Give the extent of all Plasmodium falciparum-infected red blood cells.
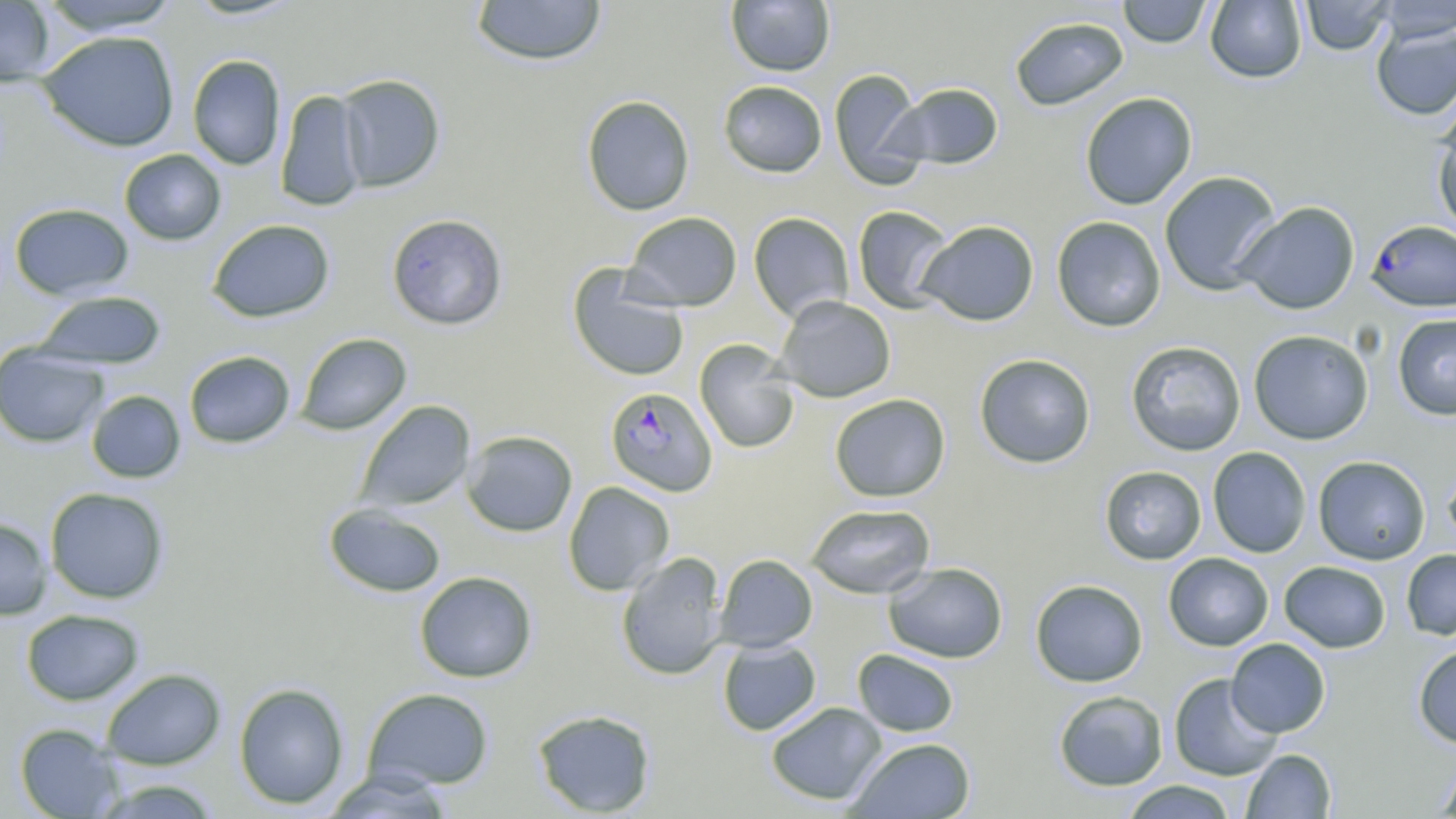

Approximate bounding boxes as (x1, y1, x2, y2) in pixels.
Plasmodium falciparum-infected red blood cells: (1365, 219, 1456, 312), (605, 387, 717, 497).

Uninfected red blood cell locations: (469, 0, 607, 67), (725, 0, 836, 76), (1118, 0, 1212, 48), (1205, 0, 1307, 83), (1299, 0, 1395, 56), (1375, 0, 1456, 42), (0, 1, 56, 86), (37, 1, 182, 35), (1009, 16, 1129, 112), (1371, 23, 1456, 120), (38, 30, 180, 152), (187, 54, 286, 170), (830, 69, 928, 186), (335, 74, 445, 192), (718, 80, 827, 177), (885, 82, 1004, 171), (275, 90, 367, 211), (1079, 92, 1198, 210), (581, 94, 696, 215), (1432, 112, 1456, 235), (119, 149, 227, 246), (1159, 171, 1282, 295), (1234, 201, 1360, 314), (9, 202, 135, 300), (852, 205, 956, 314), (623, 212, 742, 311), (748, 212, 855, 323), (386, 213, 508, 330), (1051, 216, 1167, 332), (207, 219, 335, 323), (916, 220, 1039, 326), (568, 265, 690, 382), (34, 290, 166, 370), (774, 295, 896, 402), (1392, 313, 1456, 420), (1248, 329, 1374, 445), (295, 332, 411, 435), (694, 339, 800, 454), (1126, 340, 1246, 456), (0, 344, 108, 448), (184, 350, 295, 448), (974, 353, 1096, 469), (86, 390, 186, 483), (829, 394, 951, 502), (355, 400, 475, 512), (462, 430, 577, 537), (1207, 446, 1312, 557), (1313, 455, 1431, 565), (1443, 461, 1456, 554), (1099, 465, 1206, 565), (563, 481, 675, 596), (45, 487, 169, 604), (324, 503, 447, 598), (806, 503, 936, 599), (0, 518, 52, 619), (1401, 549, 1456, 640), (615, 551, 728, 681), (1163, 553, 1273, 651), (714, 554, 818, 652), (1279, 560, 1391, 653), (883, 562, 1008, 663), (414, 571, 538, 682), (1030, 579, 1148, 687), (21, 609, 144, 705), (1225, 638, 1331, 737), (717, 640, 821, 736), (1412, 644, 1456, 748), (852, 649, 960, 737), (101, 668, 226, 769), (1168, 673, 1283, 781), (233, 682, 350, 809), (362, 687, 494, 791), (1053, 690, 1168, 791), (765, 702, 887, 805), (531, 708, 657, 816), (15, 723, 124, 818), (846, 737, 976, 818), (1241, 749, 1336, 818), (1434, 759, 1456, 817), (319, 770, 456, 818), (93, 778, 223, 818), (1121, 780, 1238, 818). Slide-level diagnosis: Plasmodium falciparum. Light microscopy. Image is 1456×819 pixels. May-Grünwald-Giemsa-stained preparation. Single field of view. Thin blood film. 1000x magnification.